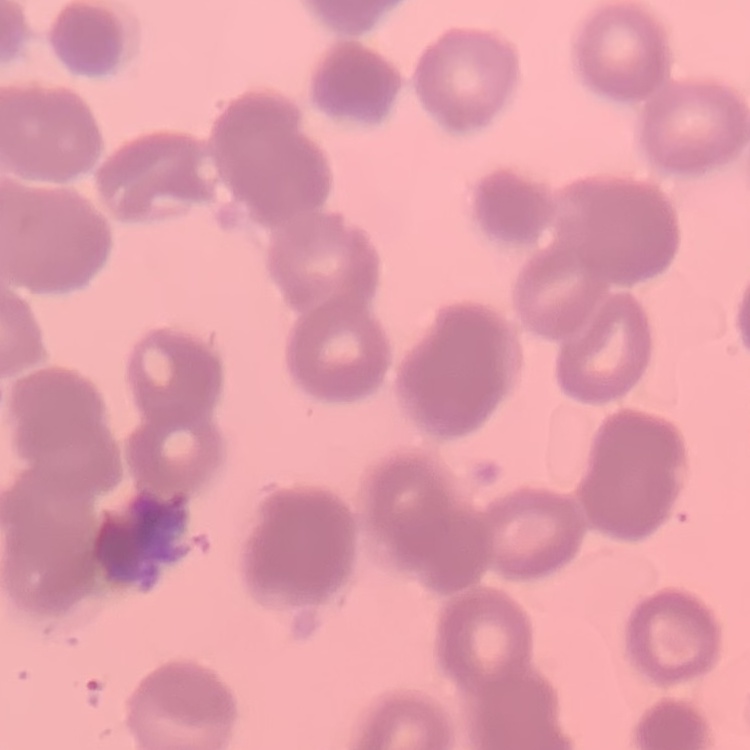

The erythrocytes exhibit rouleaux formation. Field's or Giemsa stain. Thin peripheral smear. Square crop of a larger photomicrograph.